Describe the morphology of the red blood cells.
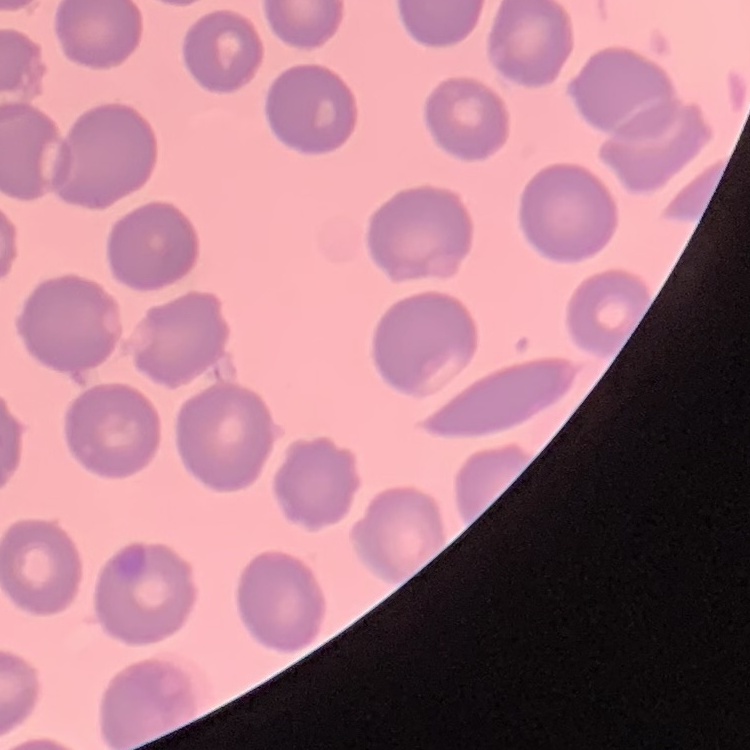
They show no rouleaux formation.

Summary:
  - Image type: one tile cut from a larger photomicrograph
  - Preparation: thin peripheral smear
  - Stain: Field's or Giemsa